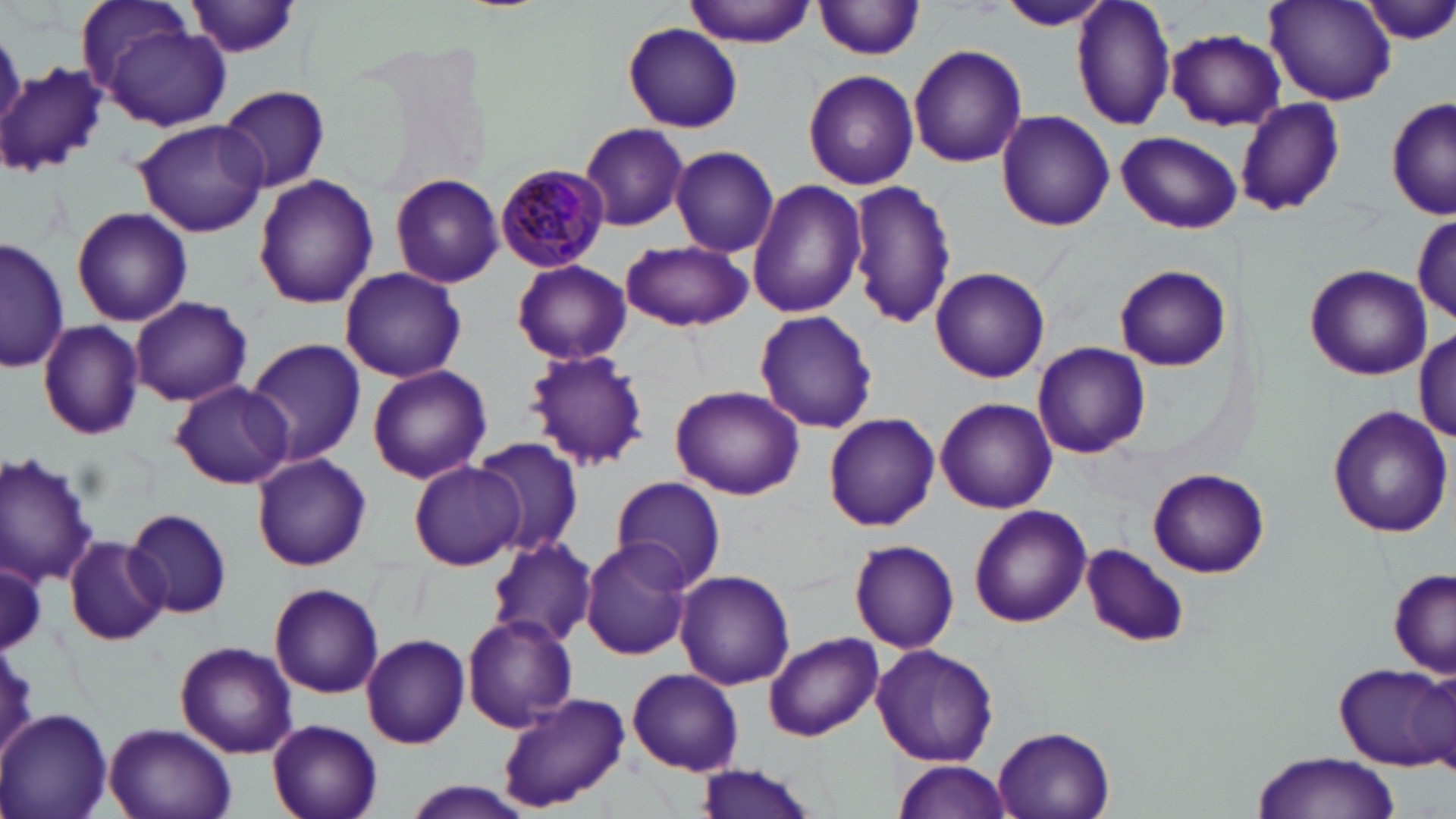

slide_level_diagnosis: Plasmodium malariae
field_of_view: single
uninfected_red_blood_cell_locations: 'approximate bounding boxes as [x1, y1, x2, y2] in pixels: [684, 0, 814, 46], [992, 0, 1116, 31], [1070, 0, 1177, 131], [1361, 0, 1456, 45], [75, 1, 199, 99], [183, 1, 303, 61], [814, 1, 926, 61], [1266, 1, 1394, 106], [623, 22, 743, 133], [105, 24, 230, 132], [1164, 30, 1284, 130], [908, 43, 1027, 169], [2, 61, 107, 177], [803, 68, 919, 190], [219, 85, 331, 193], [1387, 97, 1456, 222], [1236, 98, 1346, 218], [996, 109, 1115, 231], [131, 119, 269, 239], [578, 123, 690, 232], [1116, 130, 1243, 234], [670, 145, 780, 257], [388, 171, 504, 288], [253, 173, 379, 308], [747, 179, 869, 321], [846, 179, 957, 329], [357, 182, 489, 344], [72, 206, 192, 326], [1412, 212, 1456, 329], [0, 237, 69, 375], [620, 239, 752, 331], [513, 260, 632, 365], [1113, 263, 1232, 372], [1305, 264, 1431, 380], [340, 266, 467, 383], [931, 266, 1050, 384], [131, 295, 255, 406], [753, 310, 878, 433], [37, 321, 145, 439], [1415, 327, 1455, 443], [245, 338, 367, 467], [1031, 342, 1151, 458], [525, 350, 651, 469], [366, 363, 492, 484], [169, 381, 296, 488], [670, 385, 807, 498], [934, 397, 1056, 513], [1327, 406, 1454, 541], [824, 412, 940, 531], [472, 436, 583, 558], [0, 450, 98, 587], [251, 453, 372, 571], [408, 461, 522, 571], [1147, 467, 1270, 579], [609, 476, 728, 592], [968, 502, 1090, 627], [123, 507, 233, 619], [62, 535, 170, 645], [485, 536, 596, 647], [580, 538, 695, 660], [849, 538, 959, 653], [1080, 543, 1190, 648], [0, 561, 46, 653], [1390, 566, 1455, 677], [675, 570, 795, 690], [269, 582, 384, 698], [460, 614, 578, 731], [766, 632, 883, 740], [360, 634, 470, 749], [175, 642, 297, 758], [871, 643, 1000, 765], [1333, 660, 1455, 770], [628, 668, 744, 775], [496, 692, 629, 813], [0, 709, 113, 819], [267, 719, 383, 819], [104, 722, 235, 819], [994, 729, 1114, 819], [1251, 751, 1400, 819], [892, 760, 1012, 819], [693, 762, 820, 819], [397, 781, 535, 819]'
plasmodium_malariae_infected_red_blood_cell_locations: 'approximate bounding boxes as [x1, y1, x2, y2] in pixels: [495, 161, 610, 272]'
preparation: thin blood smear
magnification: 1000x
modality: optical microscopy
image_size: 1456×819 pixels
stain: May-Grünwald-Giemsa